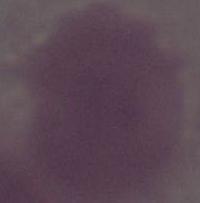

Summary:
  - Identification: red blood cell
  - Modality: photomicrograph
  - Magnification: 1000x